Classify this cell by malaria status.
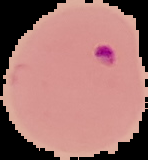

Parasitized.

image size = 148×160 pixels
image type = cell region segmented out of the field of view; surrounding area masked to black
preparation = thin blood film